Evaluate for Plasmodium parasites.
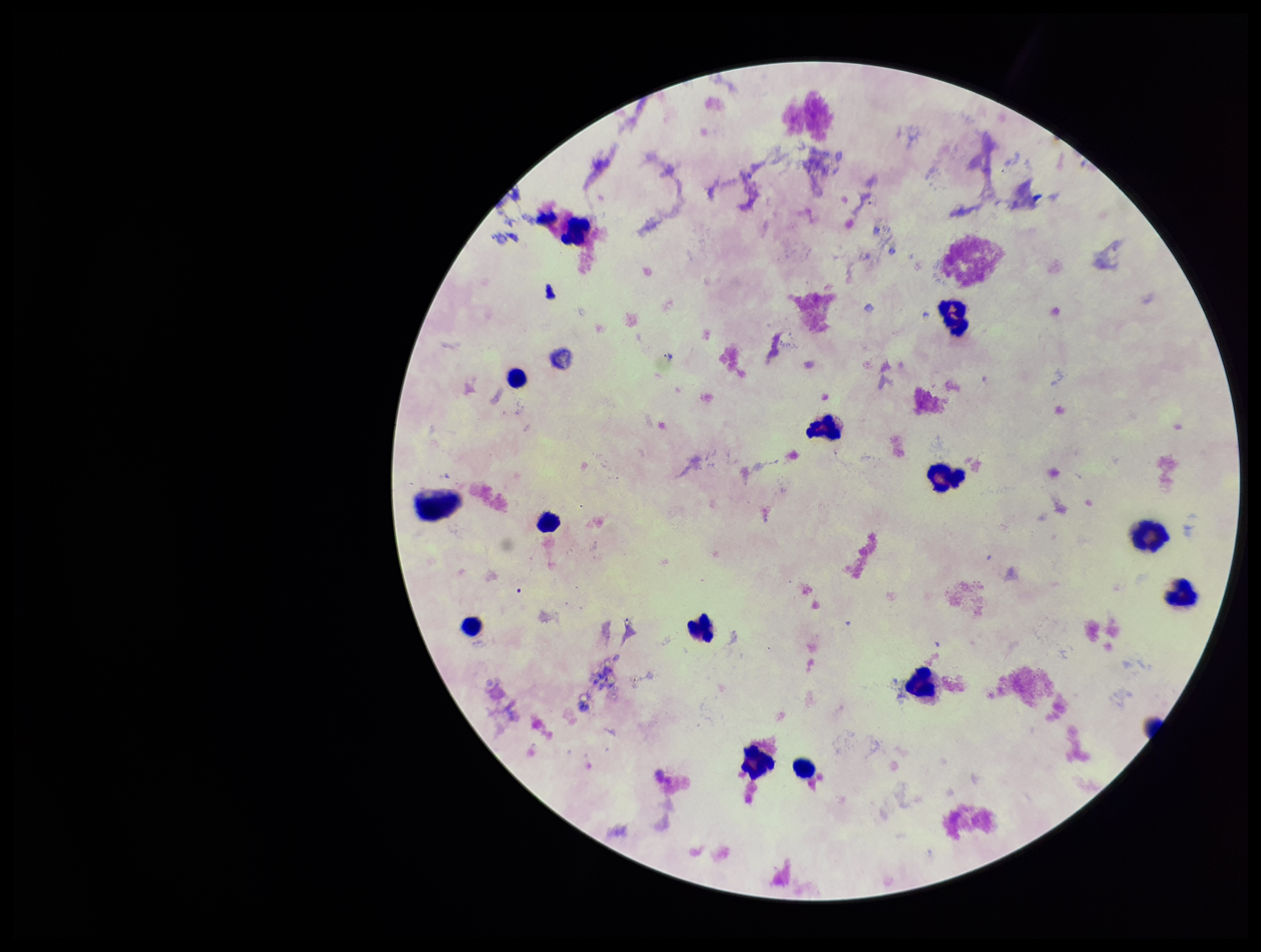
None detected.

{
  "patient_malaria_status": "negative",
  "stain": "Giemsa",
  "field_of_view": "one from this slide",
  "parasite_count": 0,
  "leukocyte_count": 15,
  "preparation": "thick blood smear",
  "capture": "smartphone photograph through the microscope eyepiece",
  "image_size": "1261×952 pixels"
}